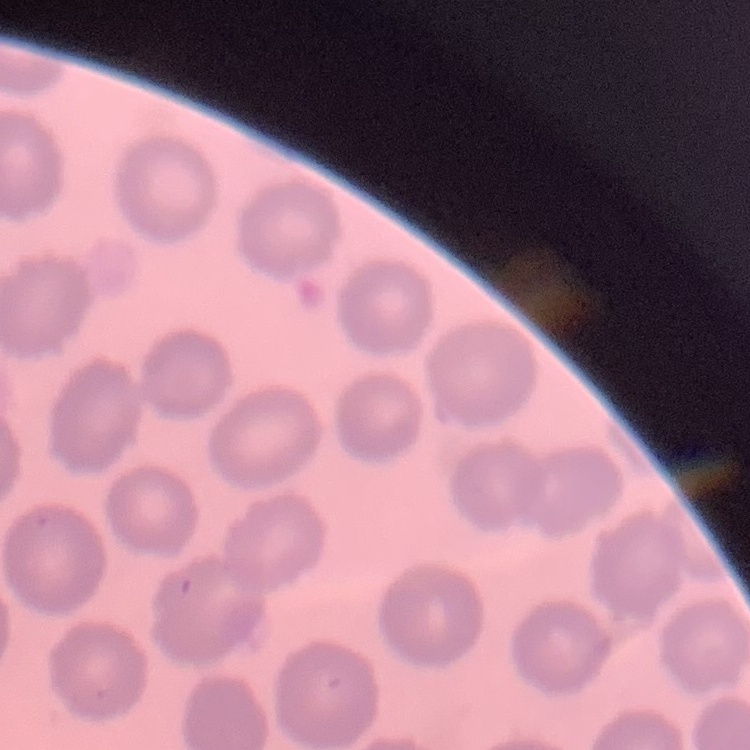

The red blood cells exhibit no rouleaux formation. Thin blood smear. One tile cut from a larger photomicrograph. Stained with either Field's or Giemsa.